Report the malaria status of this cell.
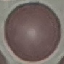
It is uninfected.

stain = Giemsa
image type = automatically extracted cell patch, resized to 64 × 64 pixels
preparation = thin smear
capture = smartphone camera at the microscope eyepiece